Name the blood parasite species.
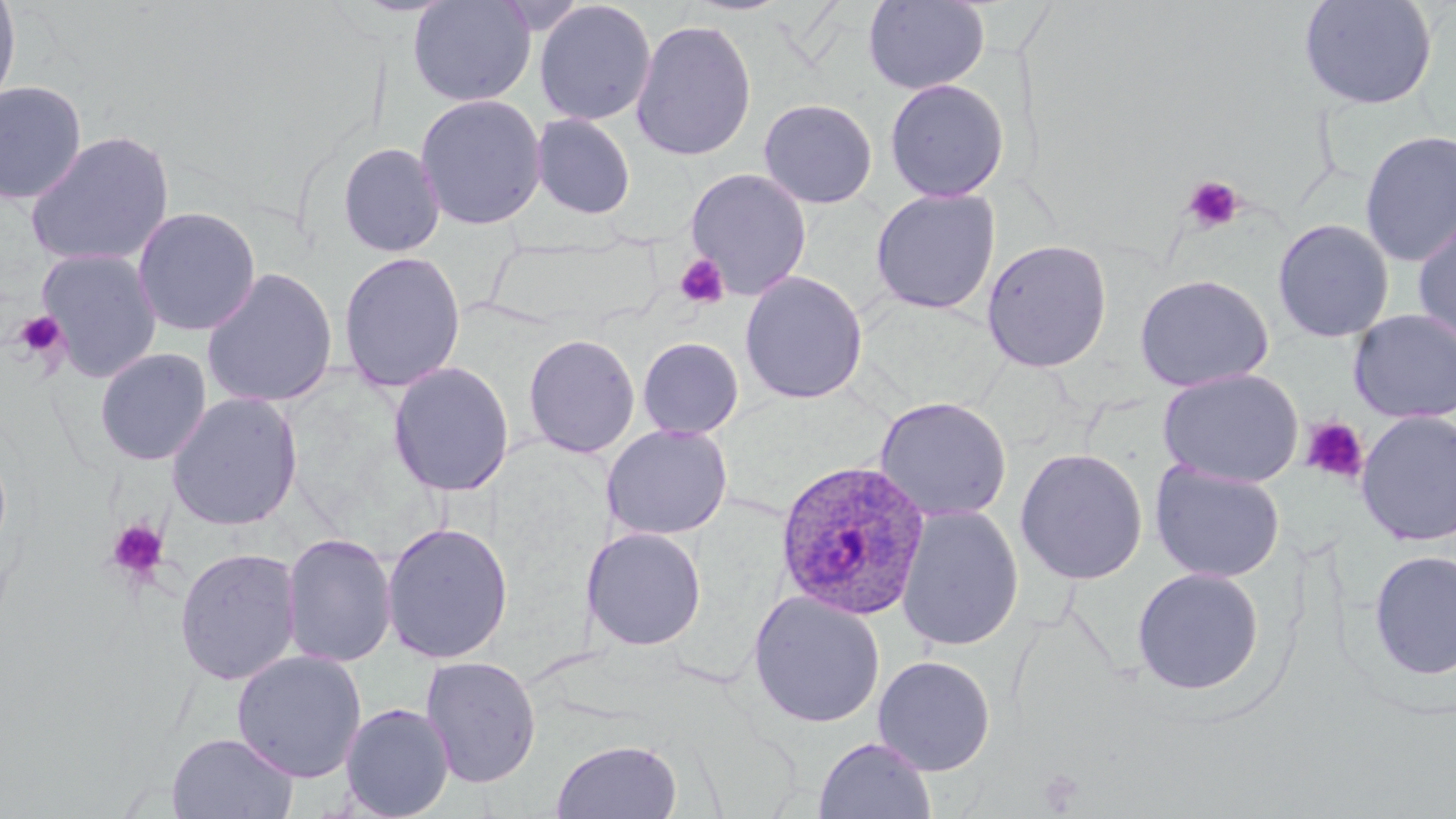
Plasmodium ovale.

Summary:
  - Coordinate format: approximate bounding boxes as (x1, y1, x2, y2) in pixels
  - Uninfected red blood cell locations: (0, 0, 21, 112), (407, 0, 537, 107), (863, 0, 990, 95), (1298, 0, 1439, 111), (534, 1, 657, 126), (630, 17, 757, 161), (884, 78, 1009, 202), (0, 80, 88, 204), (414, 94, 547, 231), (758, 97, 878, 209), (531, 112, 636, 219), (25, 129, 175, 269), (1359, 130, 1456, 267), (337, 141, 446, 257), (685, 168, 812, 300), (870, 187, 1002, 315), (131, 206, 261, 337), (1412, 213, 1456, 350), (1272, 219, 1394, 343), (981, 239, 1113, 373), (35, 248, 164, 382), (338, 250, 466, 393), (200, 266, 339, 410), (739, 271, 868, 404), (1133, 274, 1273, 392), (1348, 309, 1456, 424), (522, 333, 641, 458), (637, 336, 744, 438), (94, 347, 212, 466), (387, 361, 515, 497), (1158, 368, 1304, 487), (166, 391, 304, 531), (874, 396, 1012, 521), (1356, 410, 1456, 546), (602, 423, 733, 541), (1015, 447, 1148, 585), (1150, 462, 1286, 582), (896, 504, 1024, 651), (381, 521, 513, 664), (581, 527, 707, 651), (281, 532, 397, 668), (174, 546, 302, 687), (1369, 549, 1456, 681), (1131, 567, 1265, 695), (747, 590, 886, 729), (231, 650, 367, 783), (873, 654, 996, 775), (419, 655, 542, 788), (339, 702, 455, 819), (166, 732, 299, 818), (814, 735, 936, 819), (551, 738, 683, 819)
  - Platelet locations: (1182, 175, 1244, 233), (674, 253, 730, 309), (12, 310, 69, 362), (1300, 417, 1369, 485), (107, 518, 170, 584)
  - Plasmodium ovale-infected red blood cell locations: (775, 458, 932, 620)
  - Modality: light microscopy
  - Magnification: 1000x
  - Image size: 1456×819 pixels
  - Stain: May-Grünwald-Giemsa
  - Field of view: one of a larger specimen
  - Preparation: thin blood film